Assess the morphology of the erythrocytes.
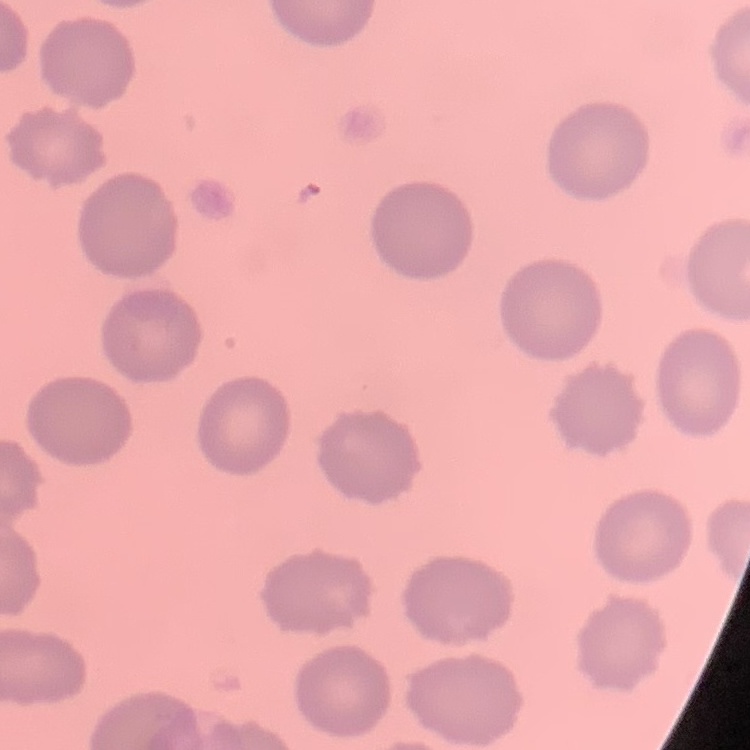
No rouleaux formation.

Summary:
  - Image type: square crop of a larger photomicrograph
  - Preparation: thin peripheral smear
  - Stain: Field's or Giemsa